Classify this cell by malaria status.
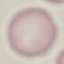

Uninfected.

image type = cell patch, automatically extracted from a larger field of view and resized to 64 × 64 pixels
preparation = thin blood smear
capture = smartphone through the microscope eyepiece
stain = Giemsa